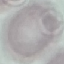
Result: no malaria parasites seen. Acquired by smartphone through the microscope eyepiece. Giemsa-stained preparation. Thin blood film. Cell patch, automatically extracted from a larger field of view and resized to 64 × 64 pixels.